State which cell type is depicted.
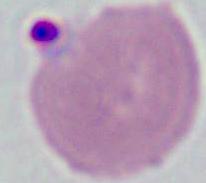

This is an erythrocyte.

magnification = 1000x
modality = micrograph